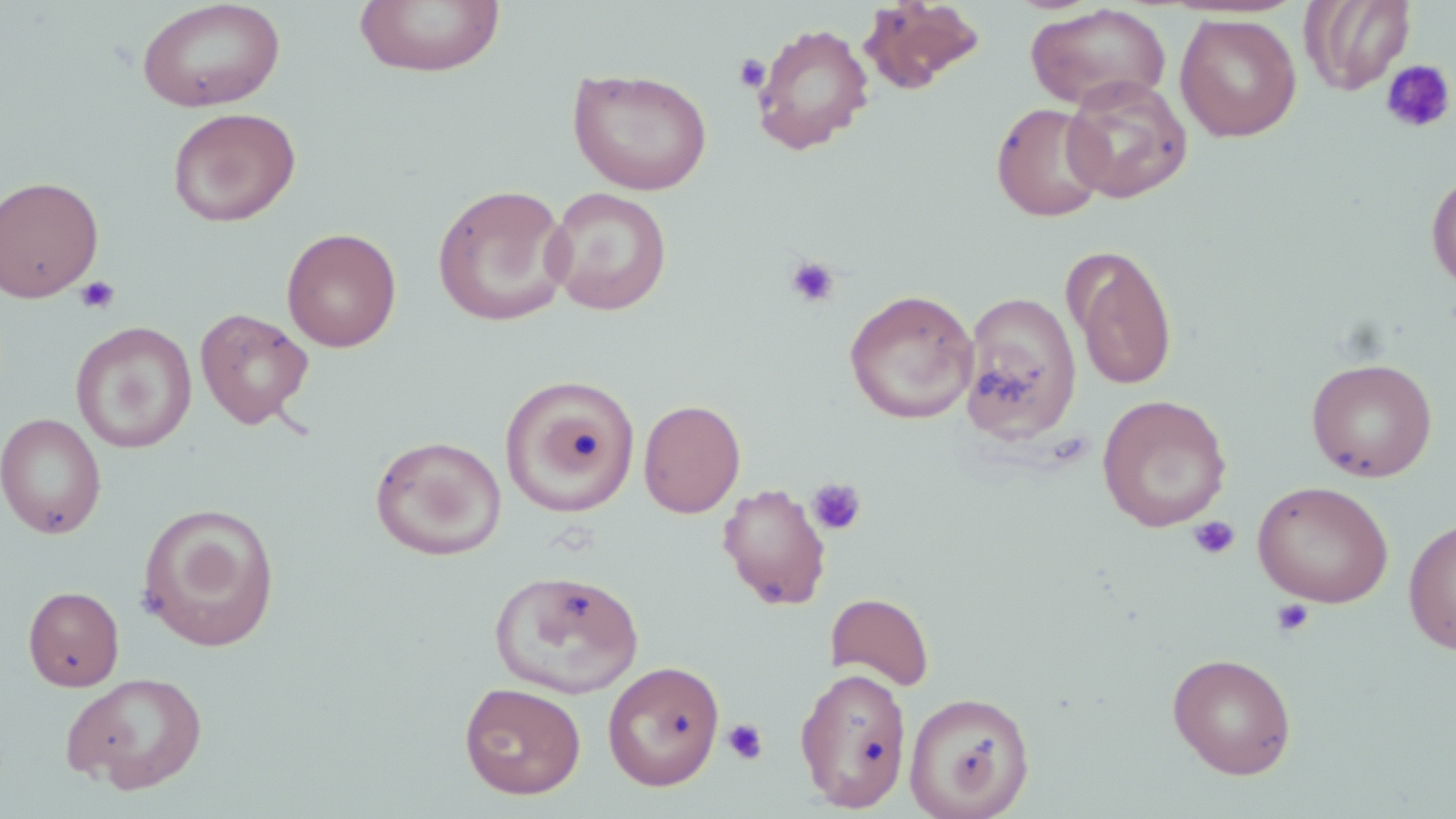
Summary:
  - Coordinate format: approximate bounding boxes as [x1, y1, x2, y2] in pixels
  - Uninfected red blood cell locations: [354, 0, 505, 78], [1301, 0, 1416, 95], [136, 1, 286, 112], [858, 1, 985, 94], [1025, 4, 1171, 112], [1175, 13, 1301, 142], [751, 22, 875, 155], [568, 67, 713, 195], [1061, 76, 1194, 203], [991, 102, 1109, 222], [167, 107, 301, 227], [1426, 169, 1456, 292], [0, 175, 104, 303], [432, 183, 573, 327], [544, 187, 673, 316], [281, 227, 402, 352], [1065, 246, 1178, 391], [844, 288, 978, 424], [959, 291, 1082, 445], [195, 307, 314, 429], [71, 322, 196, 453], [1306, 357, 1438, 482], [500, 376, 640, 519], [1097, 394, 1232, 532], [638, 398, 746, 518], [0, 412, 106, 539], [370, 435, 507, 560], [1253, 480, 1394, 607], [717, 483, 832, 610], [136, 502, 281, 651], [1403, 517, 1456, 655], [488, 567, 644, 699], [23, 586, 124, 691], [825, 592, 935, 691], [1167, 652, 1298, 779], [602, 660, 725, 790], [794, 666, 913, 812], [60, 671, 209, 793], [459, 681, 586, 799], [904, 690, 1036, 819]
  - Platelet locations: [733, 53, 771, 93], [1380, 58, 1455, 135], [784, 255, 840, 308], [75, 275, 121, 315], [806, 478, 867, 536], [1187, 515, 1240, 561], [1272, 598, 1315, 639], [722, 718, 769, 765]
  - Slide-level diagnosis: negative for blood parasites
  - Magnification: 1000x
  - Modality: optical microscopy
  - Image size: 1456×819 pixels
  - Field of view: one of a larger specimen
  - Stain: May-Grünwald-Giemsa
  - Preparation: thin blood smear